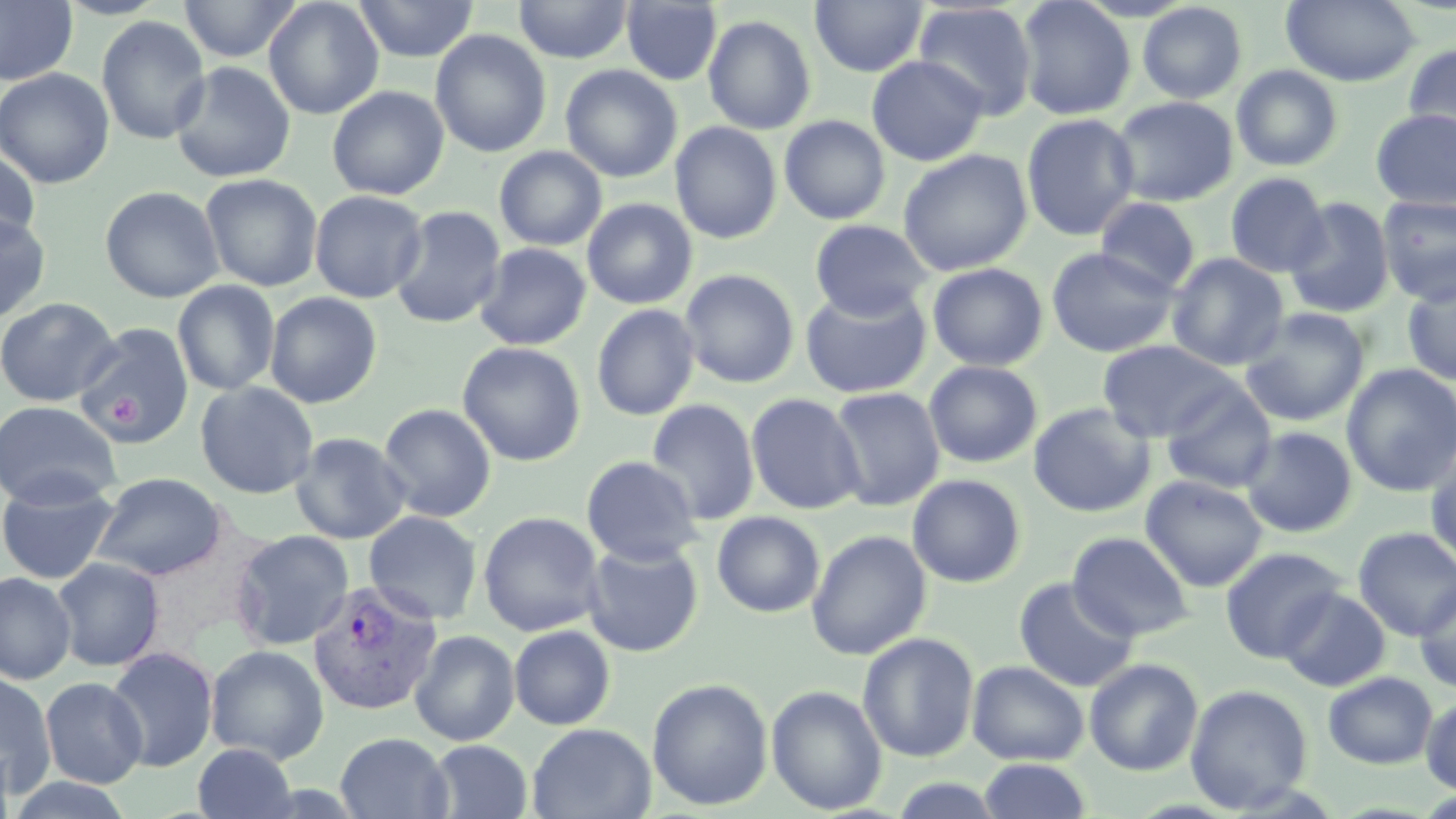 Approximate bounding boxes as [x1, y1, x2, y2] in pixels. Platelet locations: [107, 395, 144, 435]. Uninfected red blood cell locations: [0, 0, 78, 86], [55, 0, 171, 20], [178, 0, 302, 63], [263, 0, 384, 119], [353, 0, 478, 63], [513, 0, 633, 64], [1015, 0, 1136, 120], [621, 1, 723, 86], [810, 1, 928, 77], [1281, 1, 1420, 87], [913, 2, 1039, 120], [1137, 2, 1248, 104], [702, 14, 817, 134], [96, 15, 211, 145], [429, 29, 551, 159], [1402, 43, 1456, 155], [866, 56, 989, 167], [170, 61, 296, 183], [559, 64, 683, 183], [1231, 65, 1344, 172], [0, 68, 115, 189], [326, 86, 449, 200], [1110, 96, 1238, 207], [1370, 107, 1456, 211], [1021, 113, 1141, 241], [779, 115, 890, 225], [669, 121, 782, 244], [494, 146, 608, 251], [897, 148, 1033, 276], [0, 149, 41, 250], [1225, 172, 1331, 278], [199, 173, 323, 292], [99, 186, 224, 303], [309, 190, 429, 303], [1377, 195, 1456, 306], [1094, 197, 1200, 295], [1284, 197, 1396, 319], [581, 198, 698, 310], [389, 206, 507, 329], [0, 214, 51, 324], [810, 219, 932, 321], [474, 242, 591, 350], [1045, 246, 1180, 358], [1166, 253, 1289, 371], [927, 263, 1049, 371], [679, 269, 800, 388], [1401, 275, 1456, 386], [172, 279, 281, 396], [799, 284, 932, 399], [264, 292, 382, 408], [0, 297, 120, 407], [591, 304, 700, 421], [1239, 307, 1370, 426], [73, 322, 195, 448], [1097, 339, 1241, 442], [457, 341, 586, 466], [924, 360, 1043, 468], [1342, 363, 1456, 497], [195, 381, 319, 499], [1159, 381, 1278, 494], [828, 386, 945, 511], [745, 393, 866, 515], [646, 399, 760, 526], [0, 400, 122, 510], [378, 402, 497, 522], [1028, 402, 1156, 518], [1240, 425, 1358, 538], [290, 432, 411, 544], [1425, 443, 1456, 573], [581, 455, 703, 566], [91, 472, 228, 581], [907, 473, 1027, 588], [1140, 475, 1268, 592], [0, 477, 121, 584], [363, 511, 482, 625], [477, 511, 605, 637], [712, 511, 825, 618], [1353, 526, 1456, 641], [806, 529, 932, 660], [230, 530, 355, 650], [1067, 531, 1194, 641], [582, 540, 704, 657], [1219, 546, 1347, 663], [51, 557, 165, 671], [0, 571, 76, 685], [1013, 577, 1140, 693], [1414, 581, 1456, 693], [1277, 587, 1391, 692], [509, 625, 616, 730], [409, 629, 520, 746], [857, 632, 979, 762], [205, 644, 329, 765], [105, 646, 218, 772], [1084, 658, 1203, 776], [966, 660, 1089, 766], [0, 671, 56, 795], [1323, 672, 1438, 769], [40, 677, 148, 789], [646, 678, 773, 811], [765, 684, 888, 815], [1185, 684, 1313, 813], [1420, 695, 1456, 794], [527, 723, 656, 819], [335, 732, 453, 818], [427, 740, 532, 818], [0, 741, 14, 819], [192, 742, 298, 819], [977, 758, 1092, 819], [4, 776, 138, 818], [887, 777, 1007, 819]. Plasmodium vivax-infected red blood cell locations: [307, 580, 442, 716]. Slide-level diagnosis: Plasmodium vivax. May-Grünwald-Giemsa stain. Image is 1456×819 pixels. Thin blood smear. 1000x magnification. Single field of view. Optical microscopy.